Locate every blood parasite and identify its species.
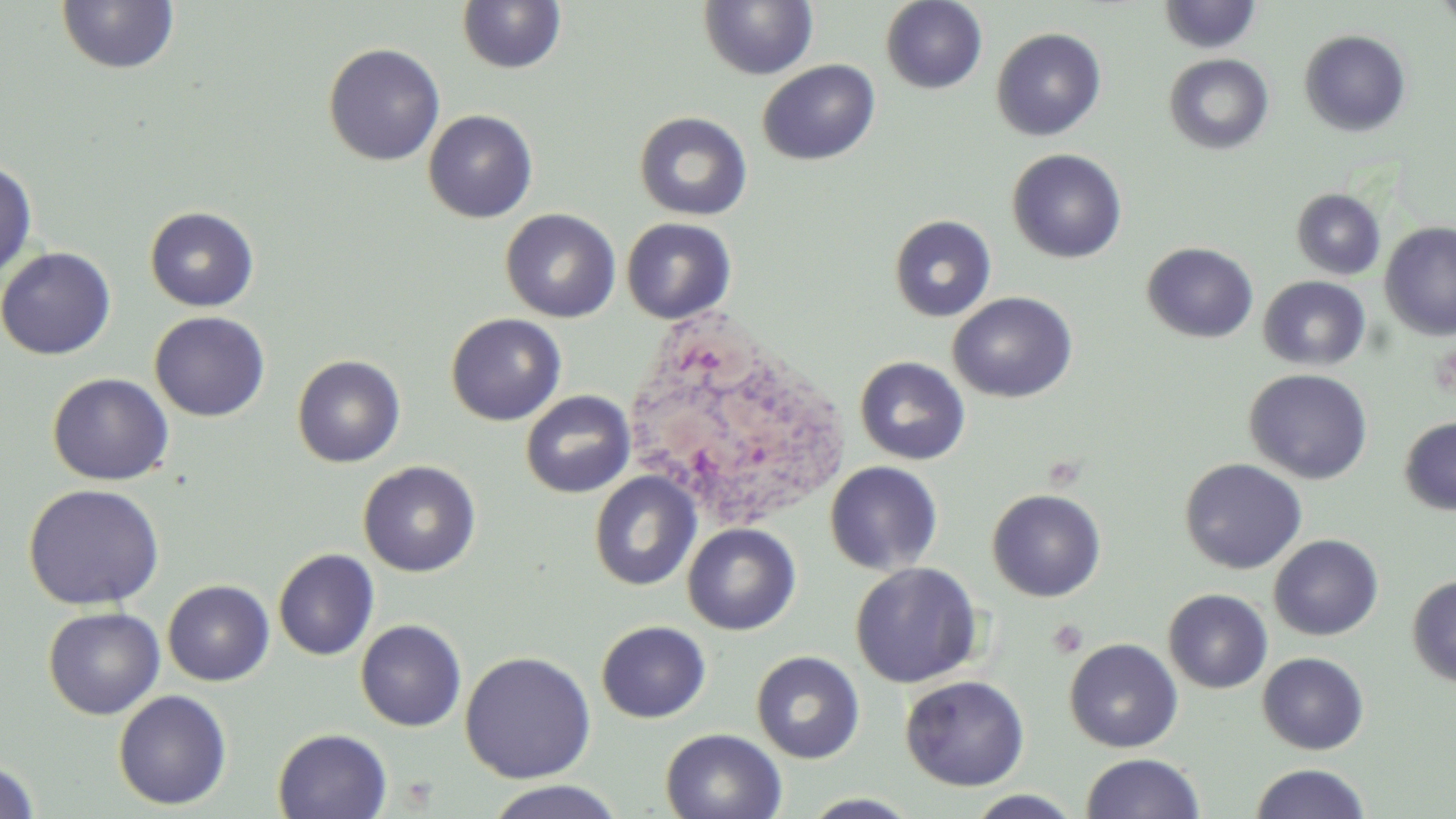
No blood parasites observed.

{
  "slide_level_diagnosis": "no evidence of blood parasites",
  "stain": "May-Grünwald-Giemsa",
  "white_blood_cell_locations": "approximate bounding boxes as (x1,y1)-(x2,y2) corner pairs in pixels: (622,302)-(854,533)",
  "magnification": "1000x",
  "uninfected_red_blood_cell_locations": "approximate bounding boxes as (x1,y1)-(x2,y2) corner pairs in pixels: (56,0)-(179,75), (880,0)-(987,94), (1433,0)-(1456,32), (456,1)-(567,74), (698,1)-(818,80), (1158,1)-(1262,55), (990,27)-(1106,141), (1299,29)-(1411,137), (323,42)-(445,166), (1163,53)-(1274,155), (757,59)-(880,166), (423,109)-(538,223), (634,111)-(753,221), (1007,149)-(1127,263), (0,159)-(38,279), (1291,188)-(1386,279), (144,206)-(259,312), (500,208)-(621,323), (888,214)-(997,322), (620,217)-(737,324), (1379,222)-(1455,340), (1142,242)-(1258,343), (0,246)-(116,360), (1258,275)-(1371,372), (948,291)-(1078,403), (149,311)-(270,422), (445,313)-(566,426), (292,354)-(406,468), (855,356)-(970,465), (1244,368)-(1373,484), (47,373)-(174,485), (520,390)-(635,498), (1399,416)-(1456,515), (1179,458)-(1307,574), (358,460)-(481,577), (825,461)-(943,575), (589,471)-(701,591), (22,483)-(165,610), (987,488)-(1106,601), (682,523)-(801,635), (1268,534)-(1384,641), (273,548)-(379,661), (850,562)-(982,687), (1407,575)-(1456,687), (162,580)-(274,686), (1164,588)-(1272,693), (43,606)-(165,719), (355,619)-(467,732), (596,620)-(710,723), (1064,638)-(1183,753), (459,650)-(596,783), (750,650)-(865,763), (1257,652)-(1369,755), (900,674)-(1030,792), (113,689)-(232,810), (273,728)-(393,819), (660,728)-(788,819), (1081,752)-(1204,819), (0,758)-(42,818), (1249,763)-(1371,819), (482,780)-(626,818), (963,790)-(1086,818), (799,792)-(923,818)",
  "modality": "light microscopy",
  "preparation": "thin blood film",
  "image_size": "1456×819 pixels",
  "platelet_locations": "approximate bounding boxes as (x1,y1)-(x2,y2) corner pairs in pixels: (1048,620)-(1088,659)",
  "field_of_view": "one of a larger specimen"
}